Outline each blood parasite and name the species.
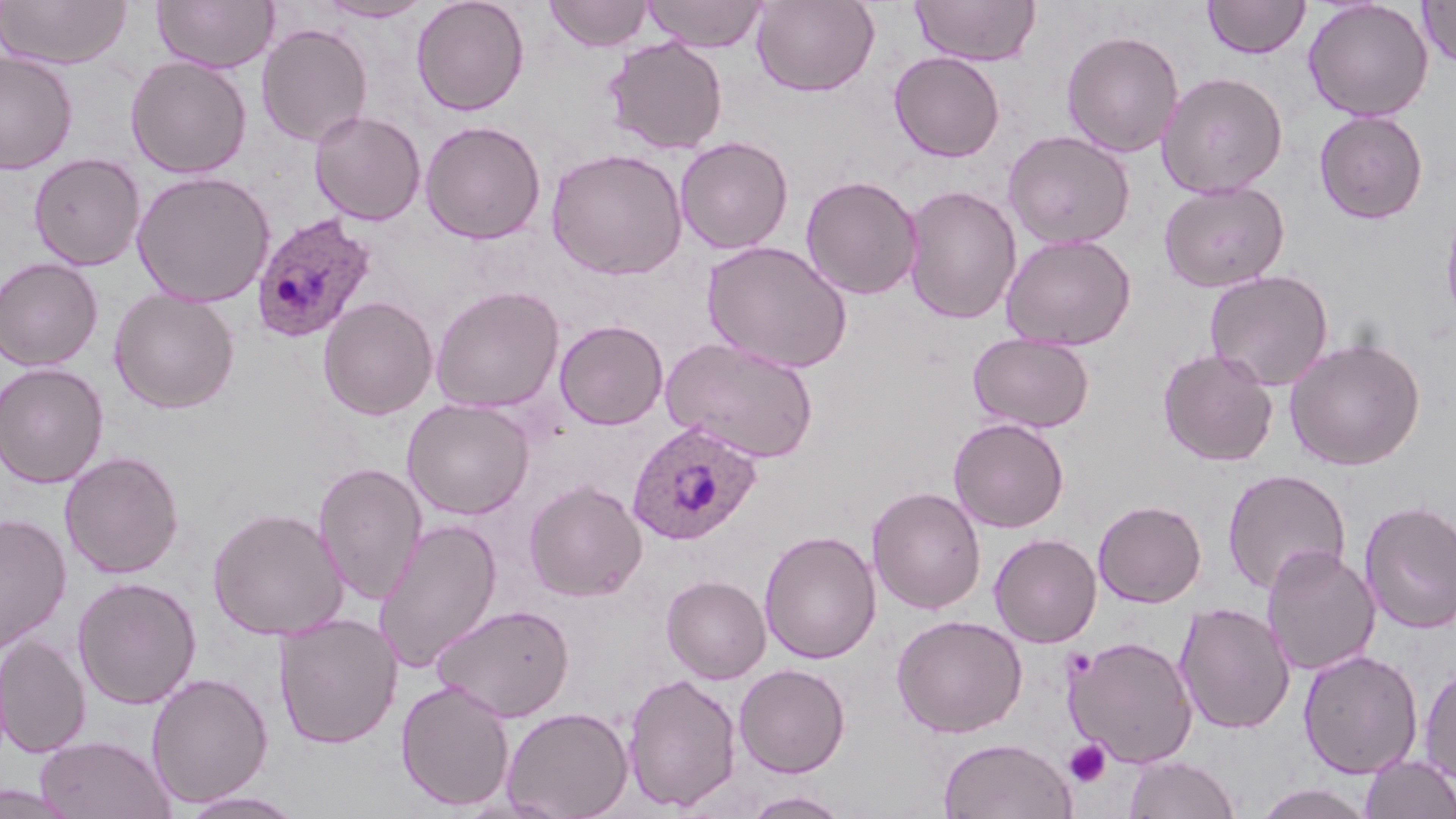

Approximate bounding boxes as named x1/y1/x2/y2 corners in pixels.
Plasmodium ovale-infected red blood cells: (x1=250, y1=212, x2=378, y2=343), (x1=627, y1=421, x2=761, y2=545).
No Plasmodium falciparum, Plasmodium malariae, Plasmodium vivax, Babesia divergens, or Trypanosoma brucei observed.

Uninfected red blood cell locations: (x1=0, y1=0, x2=132, y2=69), (x1=153, y1=0, x2=278, y2=73), (x1=317, y1=0, x2=432, y2=22), (x1=411, y1=0, x2=530, y2=116), (x1=543, y1=0, x2=654, y2=53), (x1=641, y1=0, x2=768, y2=51), (x1=751, y1=0, x2=880, y2=96), (x1=910, y1=0, x2=1041, y2=66), (x1=1203, y1=0, x2=1310, y2=59), (x1=1303, y1=0, x2=1433, y2=122), (x1=1418, y1=1, x2=1456, y2=68), (x1=256, y1=23, x2=373, y2=148), (x1=1061, y1=29, x2=1184, y2=157), (x1=603, y1=36, x2=729, y2=155), (x1=1, y1=51, x2=78, y2=175), (x1=888, y1=51, x2=1006, y2=162), (x1=125, y1=56, x2=252, y2=178), (x1=1157, y1=71, x2=1288, y2=198), (x1=309, y1=110, x2=427, y2=225), (x1=1313, y1=110, x2=1428, y2=223), (x1=419, y1=120, x2=546, y2=244), (x1=1003, y1=129, x2=1136, y2=250), (x1=674, y1=136, x2=794, y2=255), (x1=546, y1=147, x2=688, y2=280), (x1=28, y1=153, x2=145, y2=270), (x1=132, y1=170, x2=275, y2=307), (x1=800, y1=174, x2=923, y2=300), (x1=1158, y1=180, x2=1289, y2=292), (x1=901, y1=184, x2=1022, y2=325), (x1=1439, y1=192, x2=1456, y2=334), (x1=1001, y1=233, x2=1136, y2=351), (x1=701, y1=240, x2=853, y2=374), (x1=0, y1=257, x2=104, y2=371), (x1=1204, y1=270, x2=1334, y2=391), (x1=430, y1=285, x2=565, y2=414), (x1=109, y1=288, x2=240, y2=413), (x1=318, y1=296, x2=438, y2=420), (x1=554, y1=319, x2=669, y2=430), (x1=967, y1=332, x2=1095, y2=433), (x1=661, y1=335, x2=820, y2=463), (x1=1285, y1=337, x2=1426, y2=471), (x1=1157, y1=347, x2=1279, y2=467), (x1=0, y1=362, x2=109, y2=488), (x1=402, y1=398, x2=536, y2=520), (x1=948, y1=417, x2=1069, y2=533), (x1=59, y1=451, x2=184, y2=579), (x1=313, y1=461, x2=428, y2=606), (x1=1222, y1=469, x2=1351, y2=595), (x1=523, y1=480, x2=648, y2=602), (x1=867, y1=486, x2=986, y2=615), (x1=1093, y1=499, x2=1207, y2=607), (x1=1358, y1=499, x2=1456, y2=635), (x1=207, y1=506, x2=348, y2=641), (x1=0, y1=512, x2=72, y2=653), (x1=374, y1=518, x2=503, y2=672), (x1=759, y1=530, x2=882, y2=664), (x1=989, y1=532, x2=1102, y2=648), (x1=1261, y1=545, x2=1381, y2=676), (x1=661, y1=574, x2=771, y2=683), (x1=72, y1=576, x2=201, y2=709), (x1=680, y1=584, x2=813, y2=724), (x1=1174, y1=601, x2=1295, y2=735), (x1=432, y1=602, x2=575, y2=721), (x1=274, y1=612, x2=403, y2=750), (x1=891, y1=614, x2=1027, y2=738), (x1=0, y1=635, x2=92, y2=757), (x1=1064, y1=635, x2=1199, y2=768), (x1=1298, y1=649, x2=1423, y2=779), (x1=1419, y1=660, x2=1456, y2=785), (x1=734, y1=663, x2=851, y2=778), (x1=622, y1=671, x2=743, y2=814), (x1=146, y1=672, x2=274, y2=808), (x1=395, y1=678, x2=515, y2=812), (x1=501, y1=705, x2=633, y2=819), (x1=35, y1=735, x2=176, y2=819), (x1=938, y1=738, x2=1078, y2=819), (x1=1360, y1=753, x2=1456, y2=819), (x1=1123, y1=754, x2=1241, y2=819), (x1=1252, y1=783, x2=1378, y2=818), (x1=742, y1=790, x2=850, y2=818), (x1=179, y1=791, x2=307, y2=818). Platelet locations: (x1=1064, y1=739, x2=1111, y2=788). Slide-level diagnosis: Plasmodium ovale. One field of a larger specimen. Optical microscopy. Image is 1456×819 pixels. 1000x magnification. Thin blood smear. May-Grünwald-Giemsa-stained preparation.